Assess this cell for malaria.
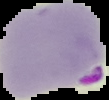
Parasitized.

From a thin blood film. Image is 109×100 pixels. The area outside the segmented cell region is set to black.